Report the malaria status of this cell.
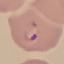
It is parasitized.

stain = Giemsa
image type = cell patch, automatically extracted from a larger field of view and resized to 64 × 64 pixels
preparation = thin blood smear
capture = smartphone through the microscope eyepiece